Name the parasite shown.
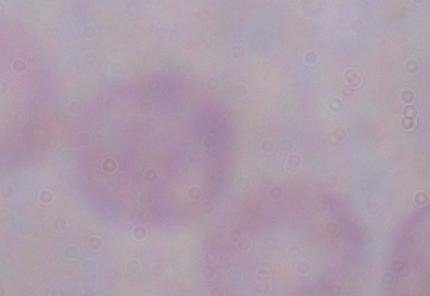
A trypanosome.

Summary:
  - Magnification: 1000x
  - Modality: photomicrograph